Assess this cell for malaria.
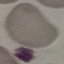

It is uninfected.

Summary:
  - Image type: automatically extracted cell patch, resized to 64 × 64 pixels
  - Capture: smartphone camera at the microscope eyepiece
  - Preparation: thin smear
  - Stain: Giemsa